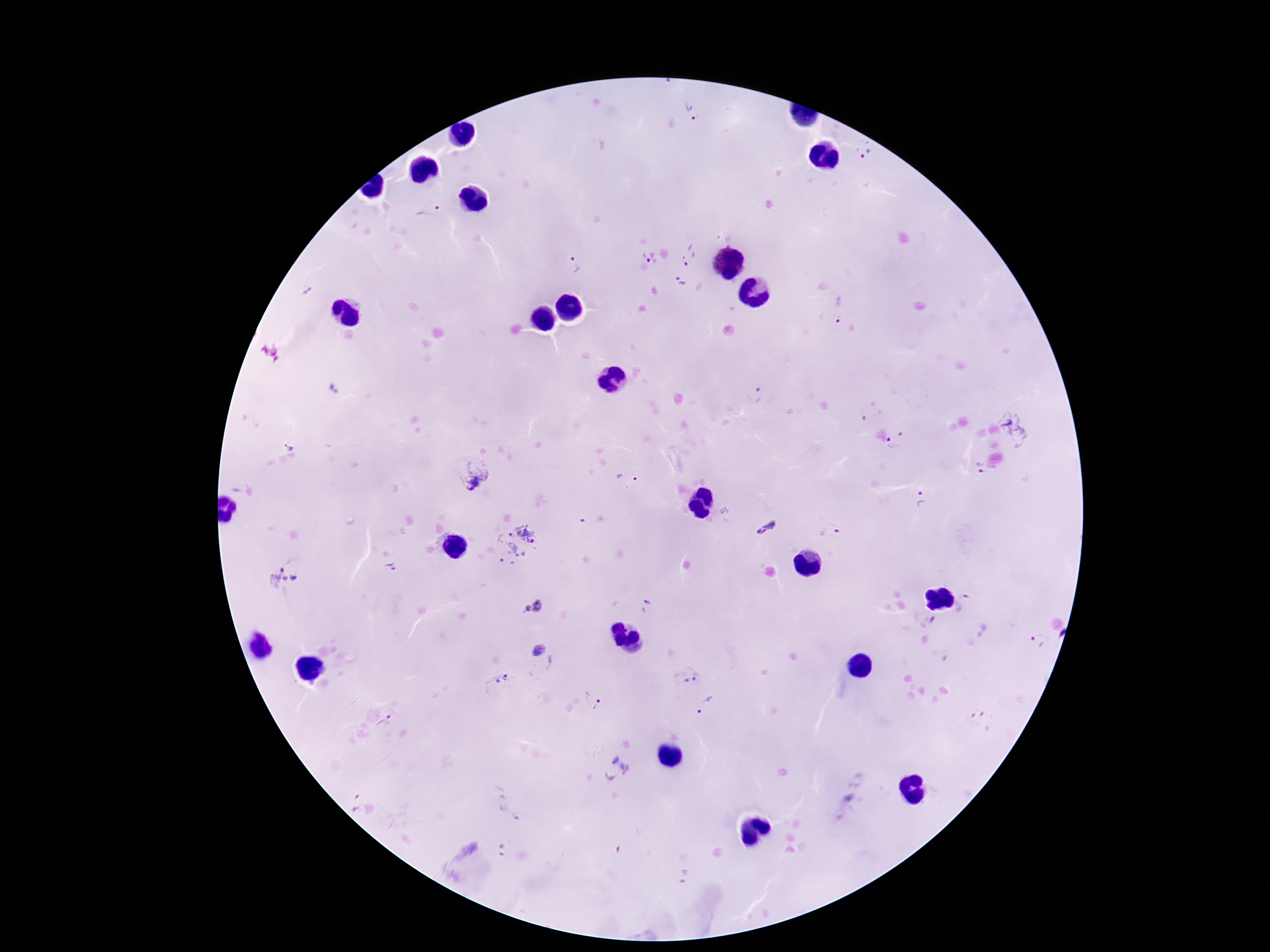

Approximate centers as {x, y} in pixels. Plasmodium parasite locations: {691, 113}, {864, 152}, {430, 213}, {688, 256}, {649, 258}, {576, 266}, {681, 281}, {307, 291}, {837, 309}, {757, 394}, {871, 414}, {1016, 428}, {897, 440}, {287, 445}, {978, 469}, {469, 472}, {626, 477}, {924, 499}, {592, 518}, {764, 528}, {832, 531}, {514, 545}, {391, 568}, {282, 578}, {647, 604}, {533, 606}, {1038, 641}, {537, 653}, {687, 675}, {499, 685}, {595, 702}, {707, 706}, {384, 722}, {617, 770}, {502, 852}, {685, 877}. Giemsa stain. Photographed through the microscope eyepiece with a smartphone camera. One field from this slide. Thick peripheral-blood smear. 100x magnification. Image is 1270×952 pixels. Patient malaria status: positive.